Locate and identify every blood parasite.
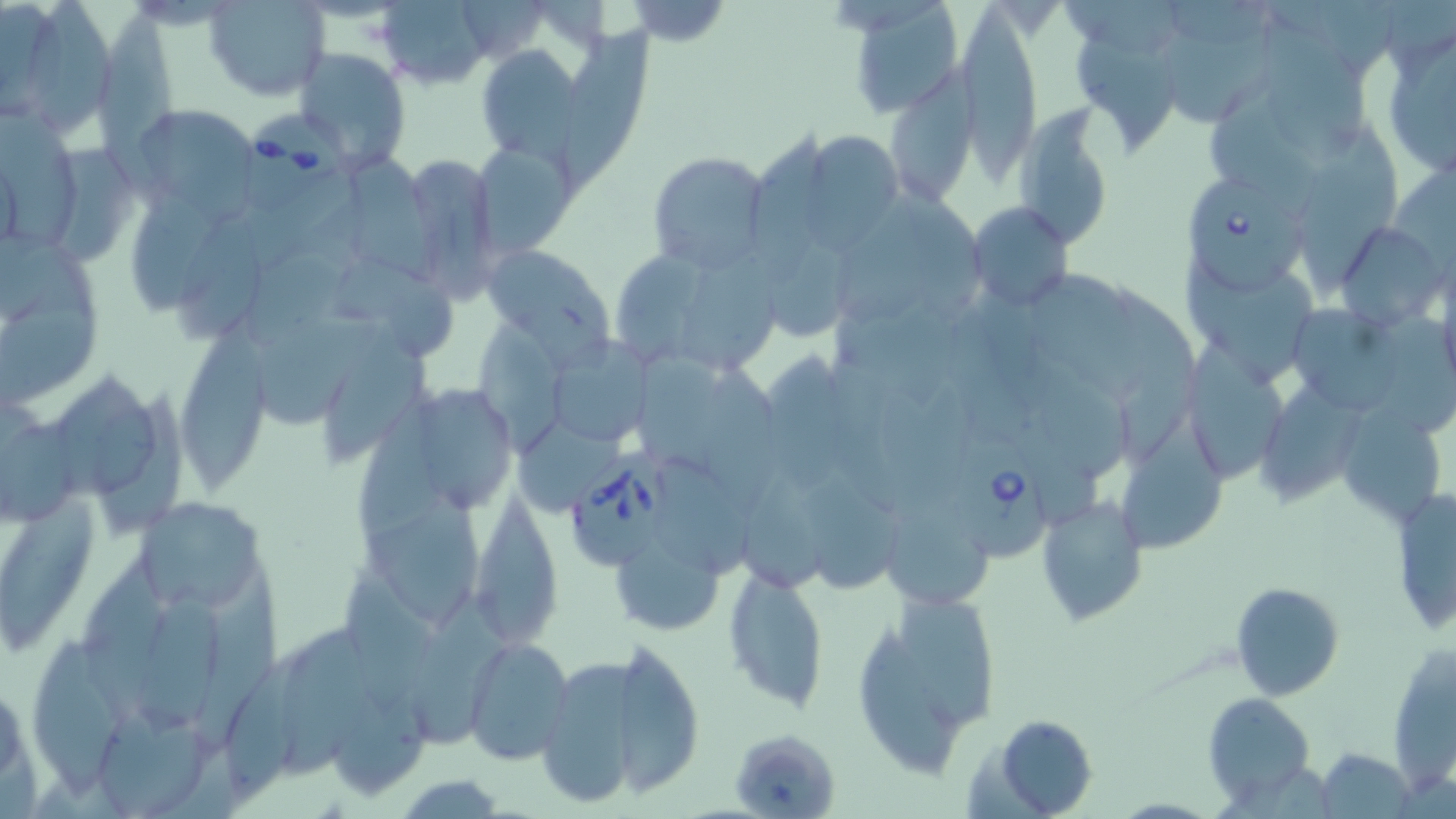
Approximate bounding boxes as (x1, y1, x2, y2) in pixels.
Babesia divergens-infected red blood cells: (245, 107, 351, 220), (1183, 165, 1314, 304), (949, 428, 1057, 565), (568, 451, 676, 570).
No Plasmodium falciparum, Plasmodium ovale, Plasmodium malariae, Plasmodium vivax, or Trypanosoma brucei observed.

slide-level diagnosis = Babesia divergens
stain = May-Grünwald-Giemsa
field of view = one of a larger specimen
preparation = thin blood film
magnification = 1000x
modality = optical microscopy
image size = 1456×819 pixels
uninfected red blood cell locations = approximate bounding boxes as (x1, y1, x2, y2) in pixels: (2, 0, 64, 117), (28, 0, 110, 136), (376, 0, 495, 88), (621, 0, 732, 47), (842, 0, 967, 117), (1056, 0, 1187, 53), (206, 1, 328, 101), (955, 5, 1043, 193), (98, 10, 185, 211), (1260, 18, 1366, 162), (1375, 18, 1456, 181), (559, 25, 659, 196), (1079, 31, 1184, 152), (475, 44, 587, 163), (294, 47, 409, 167), (886, 51, 984, 208), (1207, 82, 1323, 213), (0, 99, 79, 245), (129, 103, 260, 211), (1015, 106, 1117, 245), (750, 119, 841, 284), (1302, 123, 1400, 293), (806, 133, 903, 259), (473, 141, 579, 258), (403, 151, 501, 300), (647, 151, 771, 273), (352, 153, 445, 281), (130, 181, 222, 317), (834, 194, 930, 330), (969, 201, 1075, 313), (173, 209, 266, 341), (1334, 221, 1448, 331), (767, 233, 858, 348), (484, 245, 613, 355), (608, 248, 713, 362), (684, 250, 784, 377), (1179, 257, 1318, 391), (345, 259, 461, 357), (1034, 266, 1140, 384), (1114, 279, 1218, 441), (0, 300, 100, 409), (833, 306, 964, 405), (1296, 309, 1408, 416), (479, 310, 574, 455), (257, 313, 389, 432), (1380, 314, 1456, 439), (181, 317, 276, 490), (317, 318, 431, 459), (1177, 327, 1282, 483), (551, 337, 651, 443), (637, 345, 742, 470), (1032, 361, 1131, 475), (703, 362, 783, 511), (1264, 372, 1370, 503), (54, 374, 161, 501), (404, 380, 519, 517), (358, 386, 450, 546), (1348, 406, 1441, 523), (1119, 407, 1233, 559), (0, 417, 83, 527), (516, 419, 634, 517), (742, 466, 829, 587), (806, 477, 906, 601), (472, 488, 567, 660), (1387, 488, 1456, 636), (1, 491, 100, 654), (1034, 493, 1150, 627), (135, 495, 267, 614), (373, 499, 480, 624), (887, 512, 990, 607), (609, 530, 729, 635), (83, 554, 174, 729), (723, 563, 828, 711), (340, 565, 434, 710), (193, 579, 289, 746), (1230, 581, 1345, 701), (138, 585, 224, 733), (414, 589, 522, 749), (899, 593, 998, 726), (858, 621, 957, 772), (282, 624, 381, 777), (463, 636, 574, 766), (31, 637, 129, 801), (1388, 640, 1455, 791), (624, 642, 702, 798), (224, 645, 315, 803), (529, 645, 629, 812), (1203, 692, 1316, 808), (89, 709, 214, 819), (984, 713, 1100, 817), (733, 732, 837, 819), (1318, 746, 1417, 818), (390, 774, 516, 816)